Name the parasite shown.
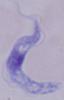
A trypanosome.

magnification: 1000x
modality: micrograph